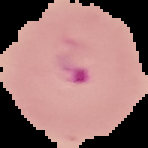
From a thin blood smear. Image is 148×148 pixels. The area outside the segmented cell region is set to black. Malaria status: parasitized.